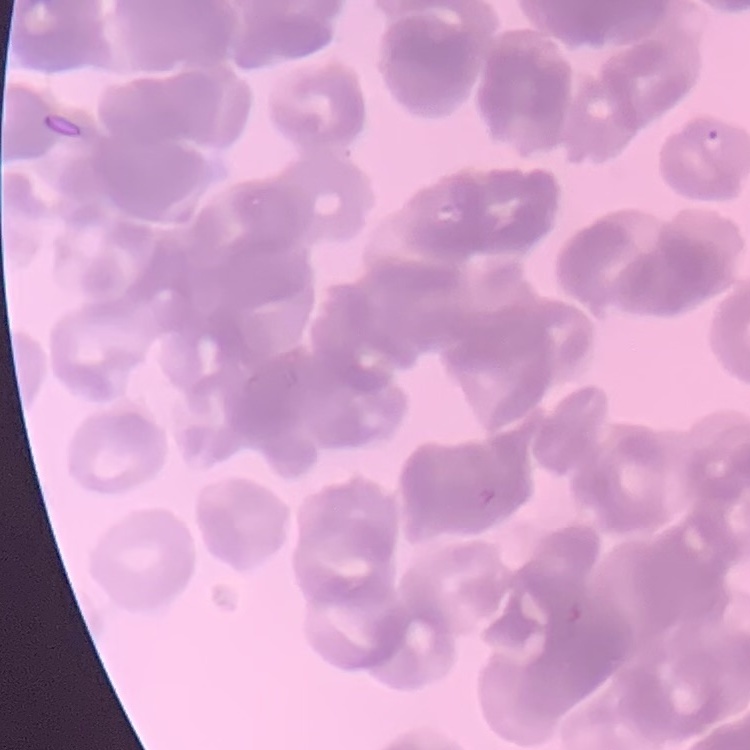

The red blood cells exhibit rouleaux formation. Stained with either Field's or Giemsa. Square crop of a larger photomicrograph. Thin blood smear.